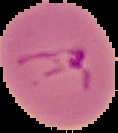 Malaria status: parasitized. Image is 118×133 pixels. From a thin blood film. Cell region segmented out of the field of view; the surrounding area is masked to black.